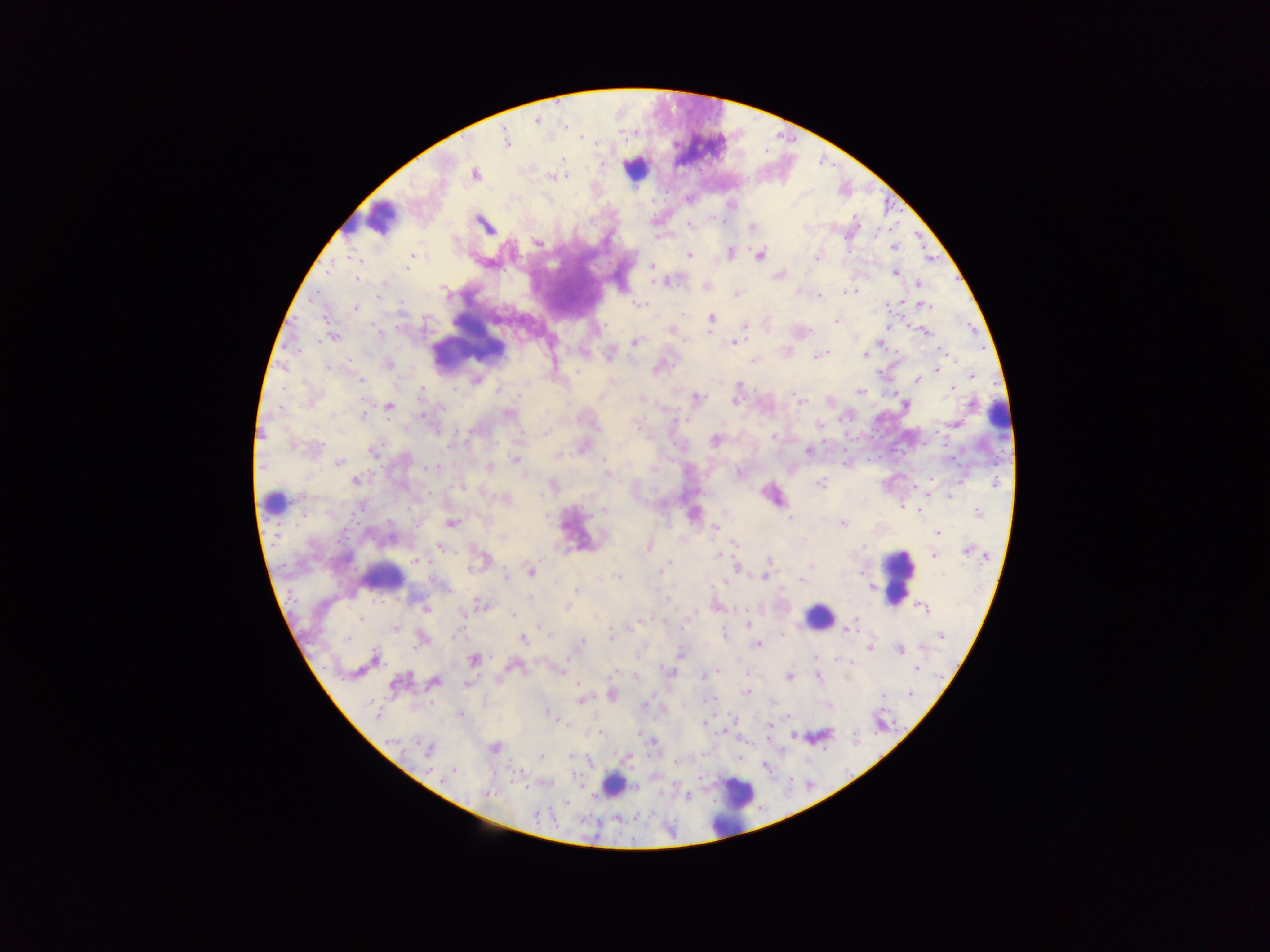
malaria parasite locations = approximate centers as (x, y) in pixels: (537, 120), (565, 126), (506, 140), (563, 159), (475, 175), (553, 177), (565, 177), (484, 224), (690, 224), (751, 227), (657, 238), (537, 242), (894, 247), (730, 252), (690, 254), (761, 256), (816, 258), (410, 260), (359, 261), (651, 266), (407, 267), (329, 270), (894, 273), (778, 275), (358, 279), (661, 282), (918, 282), (706, 287), (798, 291), (851, 291), (737, 293), (819, 296), (638, 305), (885, 305), (925, 306), (356, 307), (683, 314), (712, 318), (327, 320), (836, 320), (745, 326), (887, 326), (671, 331), (924, 332), (334, 337), (635, 342), (733, 343), (942, 351), (608, 355), (821, 355), (825, 355), (864, 355), (815, 356), (754, 360), (388, 365), (327, 368), (657, 369), (937, 369), (879, 373), (973, 375), (361, 380), (917, 380), (952, 388), (455, 389), (498, 391), (860, 392), (422, 393), (641, 398), (697, 398), (735, 400), (798, 401), (905, 405), (973, 405), (389, 406), (364, 414), (508, 414), (423, 415), (955, 424), (820, 425), (597, 428), (546, 433), (774, 436), (715, 441), (373, 451), (808, 452), (558, 455), (516, 460), (339, 463), (433, 467), (489, 467), (653, 468), (739, 473), (606, 474), (355, 481), (995, 483), (820, 484), (950, 496), (902, 507), (919, 510), (603, 511), (978, 512), (789, 518), (451, 523), (843, 524), (715, 528), (937, 533), (503, 538), (735, 543), (648, 546), (863, 547), (441, 548), (968, 551), (718, 555), (933, 555), (769, 560), (416, 561), (478, 562), (666, 566), (812, 566), (736, 567), (662, 571), (531, 572), (804, 574), (505, 576), (765, 576), (617, 577), (802, 580), (576, 590), (530, 597), (668, 599), (480, 605), (568, 606), (717, 607), (425, 609), (923, 609), (514, 615), (361, 619), (748, 624), (633, 626), (395, 628), (847, 630), (782, 634), (456, 635), (942, 635), (612, 636), (724, 636), (347, 638), (523, 639), (420, 641), (581, 641), (758, 644), (870, 648), (899, 650), (679, 653), (815, 657), (374, 659), (473, 660), (837, 660), (849, 662), (916, 668), (557, 669), (668, 671), (716, 673), (820, 673), (613, 674), (703, 676), (789, 676), (636, 677), (818, 677), (399, 682), (434, 682), (467, 684), (578, 685), (747, 692), (910, 694), (611, 696), (883, 696), (582, 699), (712, 699), (645, 704), (376, 711), (549, 713), (461, 714), (788, 716), (732, 717), (555, 718), (705, 723), (768, 726), (599, 733), (639, 735), (391, 741), (653, 743), (428, 748), (495, 748), (570, 756), (541, 757), (676, 762), (454, 771), (450, 774), (443, 778), (636, 788), (487, 794), (686, 796), (537, 815)
country = Ghana
preparation = thick blood smear
image size = 1270×952 pixels
field of view = single
leukocyte locations = approximate centers as (x, y) in pixels: (634, 168), (379, 218), (465, 338), (997, 416), (273, 503), (897, 575), (381, 576), (818, 617), (612, 784), (733, 805)
capture = mobile-phone photograph through a microscope